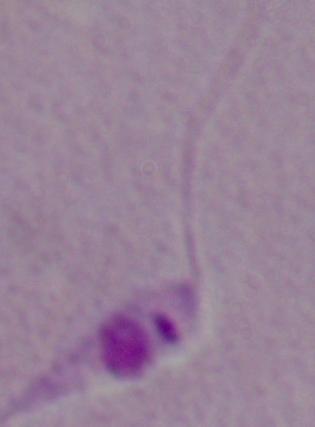
identification = Leishmania
modality = photomicrograph
magnification = 1000x